State the blood parasite species.
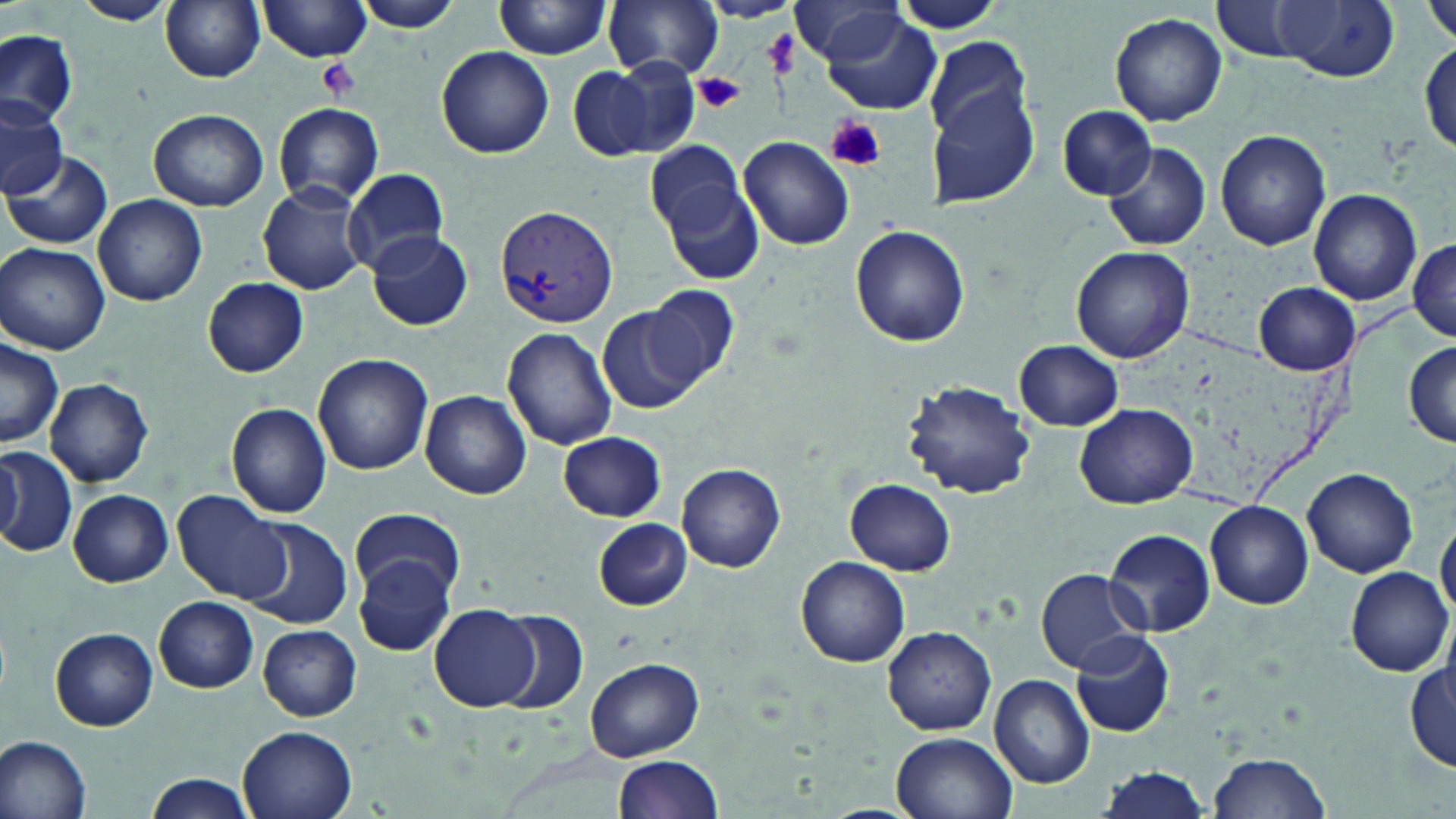
Plasmodium vivax.

Approximate bounding boxes as named x1/y1/x2/y2 corners in pixels. Platelet locations: (x1=763, y1=29, x2=796, y2=79), (x1=317, y1=58, x2=361, y2=100), (x1=696, y1=73, x2=744, y2=112), (x1=823, y1=114, x2=885, y2=173). Uninfected red blood cell locations: (x1=356, y1=0, x2=465, y2=33), (x1=605, y1=0, x2=723, y2=81), (x1=884, y1=0, x2=1009, y2=34), (x1=1209, y1=0, x2=1316, y2=62), (x1=1422, y1=0, x2=1456, y2=45), (x1=73, y1=1, x2=174, y2=26), (x1=160, y1=1, x2=266, y2=82), (x1=259, y1=1, x2=373, y2=62), (x1=493, y1=1, x2=613, y2=59), (x1=698, y1=1, x2=799, y2=23), (x1=1275, y1=1, x2=1400, y2=81), (x1=792, y1=2, x2=907, y2=66), (x1=820, y1=10, x2=943, y2=115), (x1=1110, y1=12, x2=1228, y2=127), (x1=0, y1=30, x2=77, y2=125), (x1=924, y1=36, x2=1036, y2=145), (x1=1416, y1=36, x2=1456, y2=152), (x1=436, y1=46, x2=554, y2=159), (x1=565, y1=59, x2=667, y2=157), (x1=927, y1=83, x2=1043, y2=209), (x1=0, y1=93, x2=68, y2=200), (x1=273, y1=103, x2=386, y2=205), (x1=1058, y1=106, x2=1157, y2=200), (x1=149, y1=109, x2=268, y2=210), (x1=1216, y1=129, x2=1332, y2=251), (x1=739, y1=135, x2=853, y2=249), (x1=645, y1=140, x2=744, y2=241), (x1=1104, y1=141, x2=1210, y2=250), (x1=6, y1=149, x2=112, y2=250), (x1=343, y1=168, x2=448, y2=276), (x1=663, y1=176, x2=764, y2=289), (x1=257, y1=181, x2=370, y2=295), (x1=1308, y1=189, x2=1422, y2=307), (x1=93, y1=194, x2=207, y2=307), (x1=851, y1=226, x2=969, y2=347), (x1=368, y1=230, x2=472, y2=331), (x1=1408, y1=238, x2=1456, y2=341), (x1=1, y1=243, x2=110, y2=354), (x1=1070, y1=245, x2=1195, y2=364), (x1=203, y1=277, x2=308, y2=377), (x1=1253, y1=282, x2=1358, y2=375), (x1=641, y1=284, x2=738, y2=388), (x1=597, y1=306, x2=701, y2=413), (x1=502, y1=327, x2=617, y2=451), (x1=1013, y1=339, x2=1122, y2=430), (x1=0, y1=340, x2=63, y2=447), (x1=1403, y1=342, x2=1456, y2=447), (x1=313, y1=353, x2=433, y2=475), (x1=45, y1=377, x2=154, y2=487), (x1=903, y1=380, x2=1035, y2=499), (x1=420, y1=390, x2=532, y2=499), (x1=1074, y1=402, x2=1197, y2=509), (x1=226, y1=403, x2=332, y2=518), (x1=559, y1=431, x2=666, y2=520), (x1=0, y1=447, x2=75, y2=559), (x1=1, y1=452, x2=26, y2=546), (x1=677, y1=465, x2=785, y2=572), (x1=1302, y1=468, x2=1418, y2=577), (x1=846, y1=478, x2=956, y2=574), (x1=67, y1=489, x2=174, y2=586), (x1=173, y1=490, x2=291, y2=605), (x1=1206, y1=502, x2=1314, y2=609), (x1=349, y1=507, x2=464, y2=602), (x1=240, y1=517, x2=354, y2=630), (x1=592, y1=517, x2=692, y2=611), (x1=1436, y1=517, x2=1456, y2=622), (x1=1104, y1=528, x2=1215, y2=637), (x1=353, y1=556, x2=456, y2=658), (x1=796, y1=556, x2=910, y2=667), (x1=1345, y1=567, x2=1452, y2=674), (x1=1035, y1=568, x2=1147, y2=673), (x1=154, y1=597, x2=258, y2=692), (x1=432, y1=605, x2=538, y2=711), (x1=495, y1=612, x2=588, y2=714), (x1=258, y1=624, x2=361, y2=721), (x1=883, y1=625, x2=996, y2=735), (x1=51, y1=627, x2=158, y2=730), (x1=1070, y1=631, x2=1175, y2=738), (x1=1405, y1=657, x2=1456, y2=771), (x1=586, y1=658, x2=706, y2=760), (x1=990, y1=673, x2=1096, y2=788), (x1=234, y1=723, x2=360, y2=819), (x1=890, y1=732, x2=1016, y2=819), (x1=0, y1=735, x2=92, y2=816), (x1=1208, y1=751, x2=1331, y2=818), (x1=612, y1=755, x2=723, y2=819), (x1=1094, y1=767, x2=1209, y2=818), (x1=144, y1=773, x2=256, y2=819). Plasmodium vivax-infected red blood cell locations: (x1=496, y1=206, x2=618, y2=329). 1000x magnification. May-Grünwald-Giemsa-stained preparation. One field of a larger specimen. Image is 1456×819 pixels. Optical microscopy. Thin blood film.